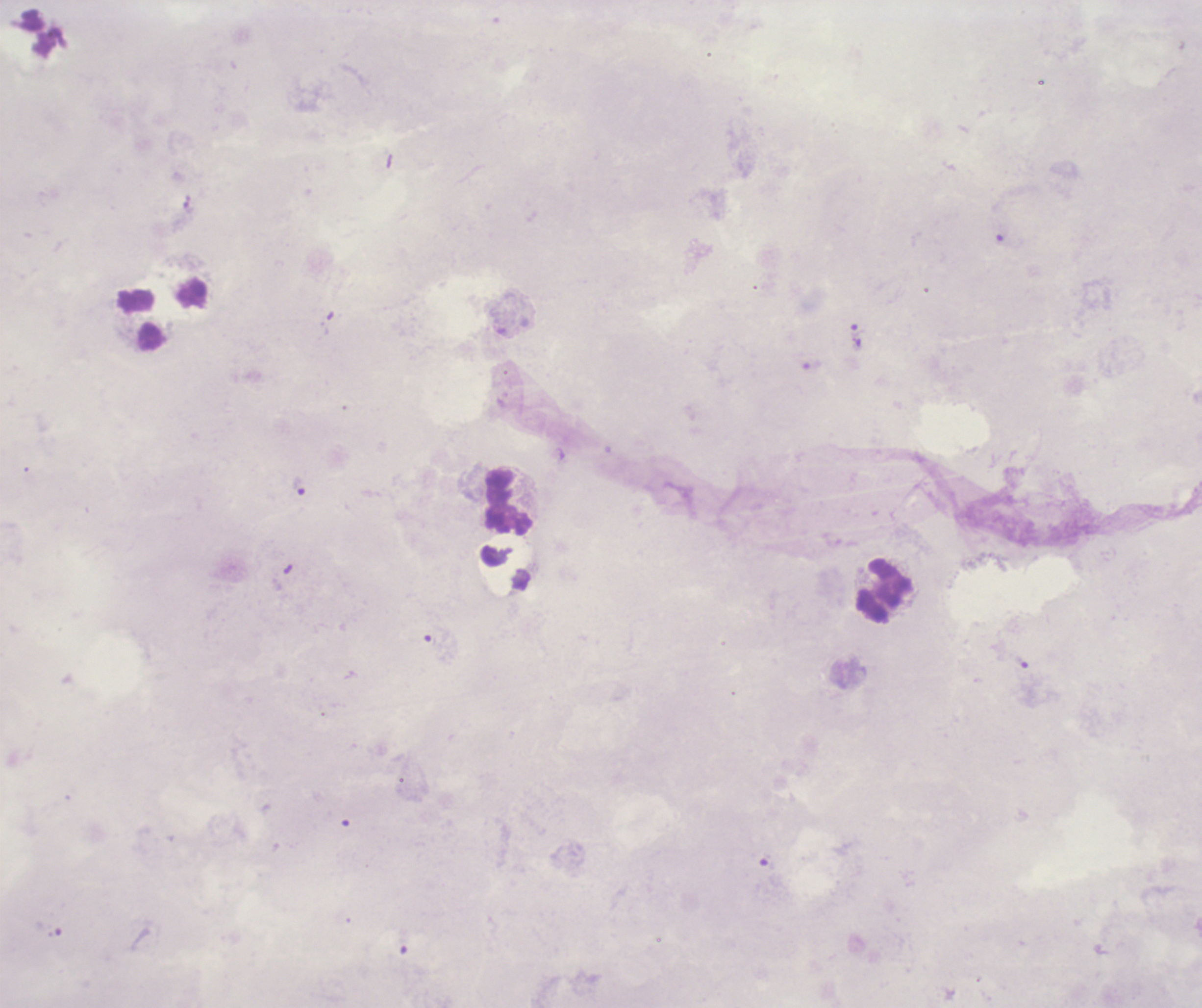

Approximate object centers, in pixels from the top-left corner.
Summary:
  - Trophozoite locations: (x=858, y=330), (x=300, y=486), (x=1022, y=662), (x=767, y=862)
  - Leukocyte locations: (x=142, y=321), (x=509, y=504), (x=883, y=590)
  - Result: positive for malaria parasites
  - Preparation: thick smear of blood
  - Context: previously used in an actual diagnosis
  - Stain: Romanowsky
  - Background quality: poor
  - Coloration quality: bad
  - Image size: 1202×1008 pixels
  - Magnification: 100x
  - Field of view: one from this slide